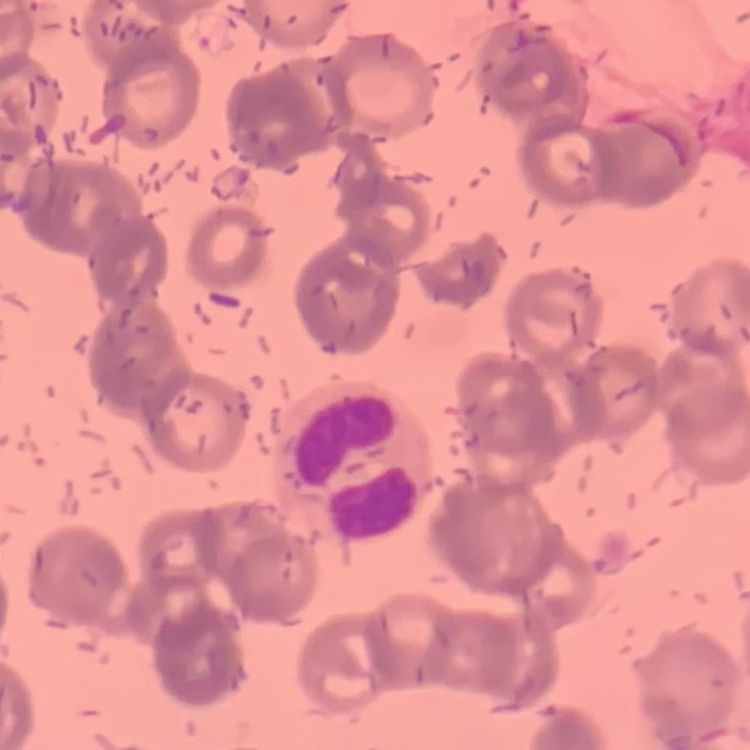

Summary:
  - Red blood cell morphology: rouleaux formation
  - Preparation: thin peripheral smear
  - Stain: Field's or Giemsa
  - Image type: square crop of a larger photomicrograph